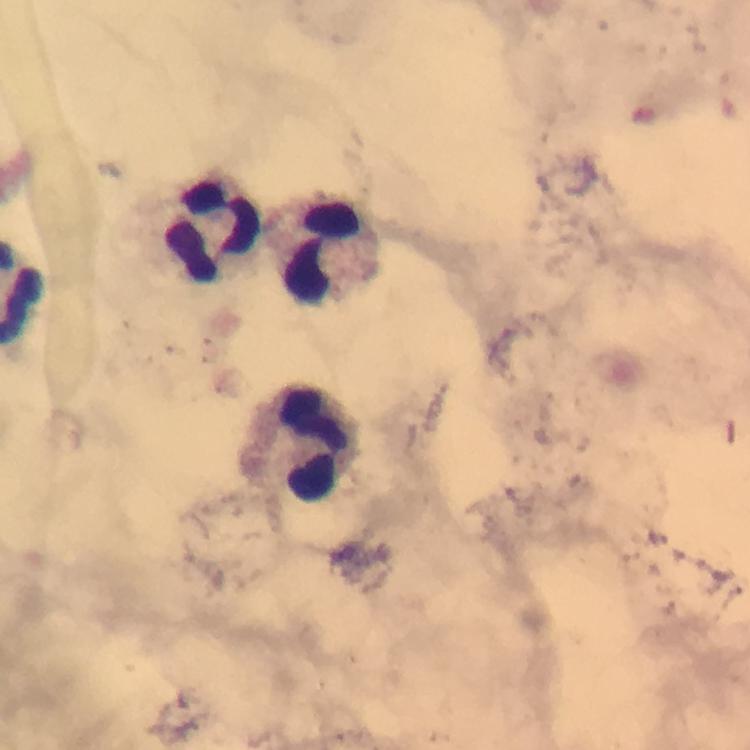

preparation = thick smear
image size = 750×750 pixels
context = from a malaria diagnostic workup
immersion oil = used
magnification = 100x
capture = smartphone camera through the microscope
leukocyte locations = approximate centers as [x, y] in pixels: [214, 231], [320, 252], [310, 448]
stain = Giemsa
cropped from = one field of view
malaria parasites = none detected